Point out each Plasmodium parasite.
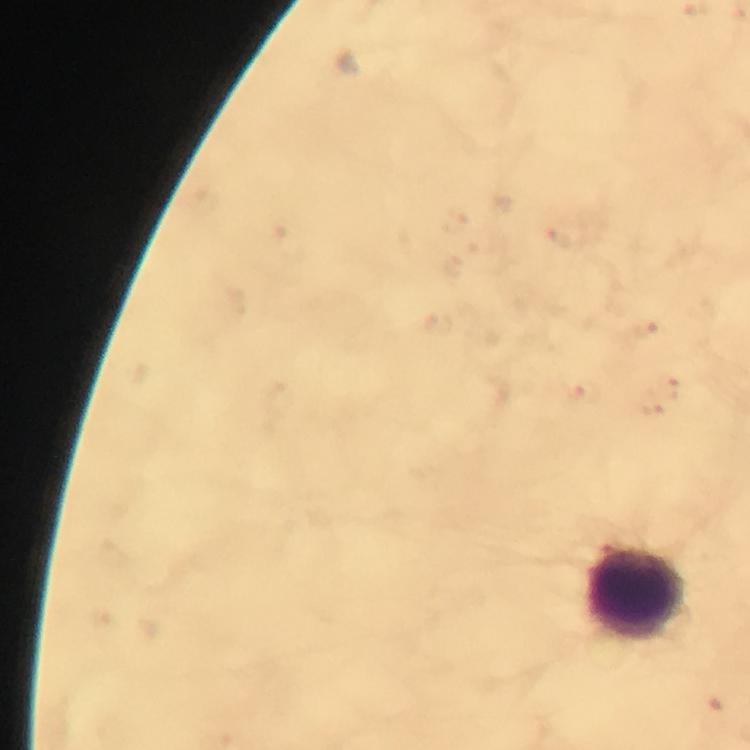

No Plasmodium parasites seen.

stain: Giemsa
magnification: 100x
immersion_oil: applied
context: from a malaria diagnostic workup
capture: smartphone mounted on the microscope
image_size: 750×750 pixels
leukocyte_locations: 'approximate centers as {x, y} in pixels: {638, 594}'
preparation: thick smear
cropped_from: a single field of view